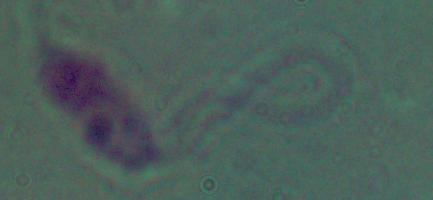
{
  "magnification": "1000x",
  "modality": "photomicrograph",
  "identification": "Leishmania"
}